Name the parasite shown.
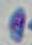
This is Toxoplasma gondii.

modality = photomicrograph
magnification = 1000x